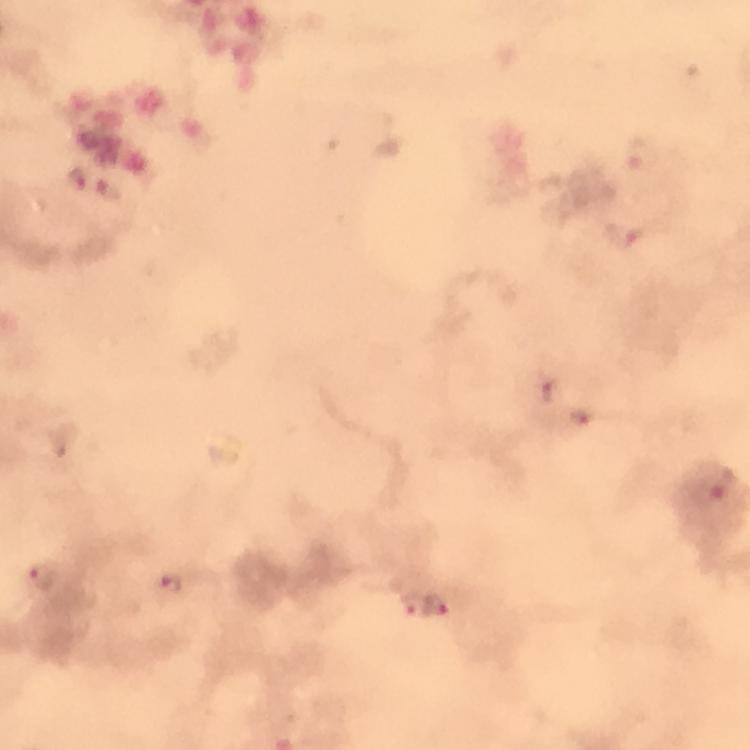

Approximate object centers, in pixels from the top-left corner. Malaria parasite locations: (x=77, y=178), (x=109, y=189), (x=627, y=234), (x=547, y=389), (x=583, y=416), (x=43, y=576), (x=172, y=583), (x=410, y=602), (x=437, y=605). Photographed with a smartphone mounted on the microscope. Image is 750×750 pixels. Immersion oil applied. From a malaria diagnostic workup. Giemsa stain. Thick blood smear. 100x magnification. A crop from one field of view.